State the blood parasite species.
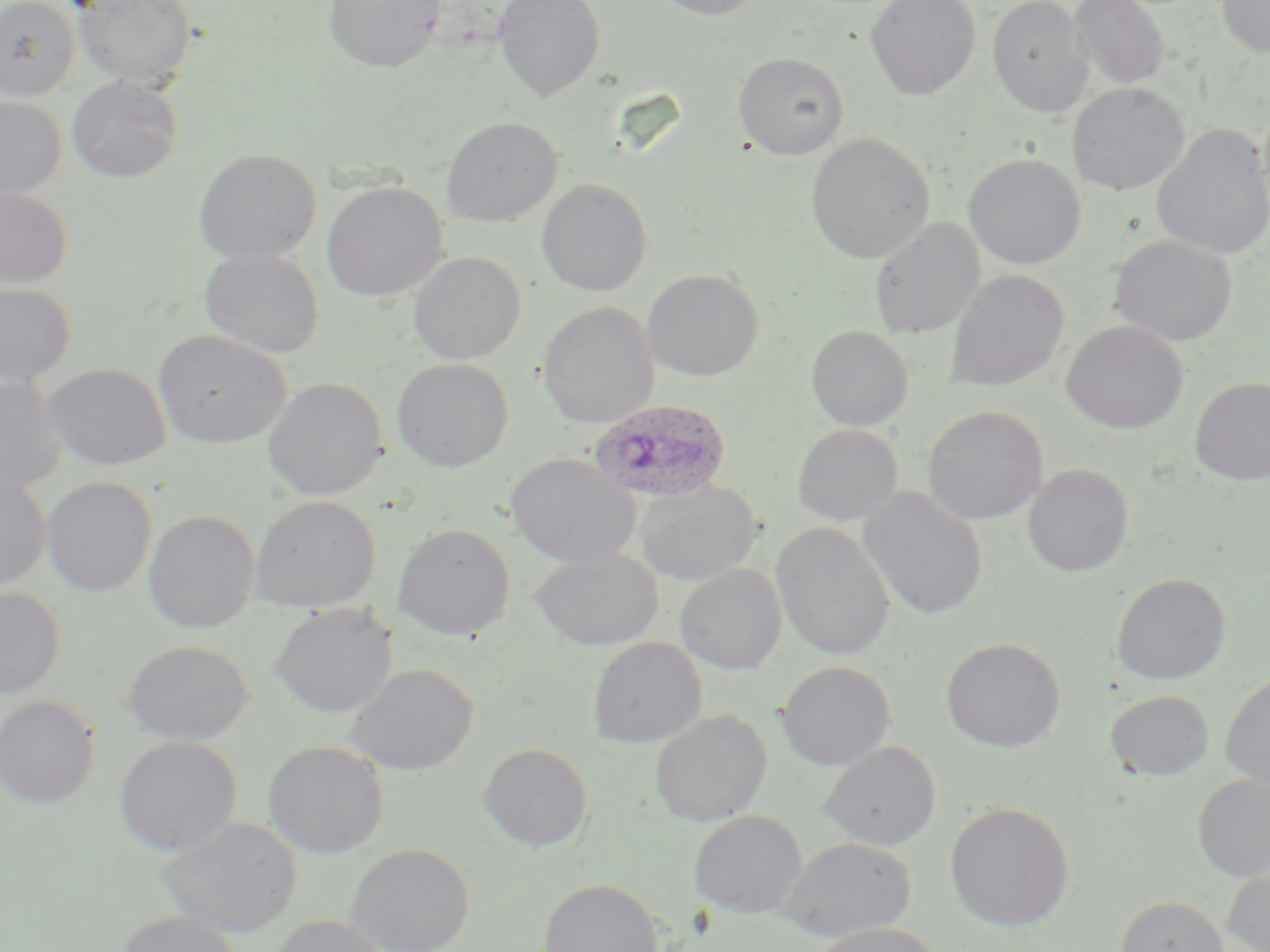

Plasmodium ovale.

Summary:
  - Coordinate format: approximate bounding boxes as (x1, y1, x2, y2) in pixels
  - Uninfected red blood cell locations: (0, 0, 80, 101), (73, 0, 197, 89), (323, 0, 446, 74), (493, 0, 605, 102), (648, 0, 768, 20), (865, 0, 981, 100), (986, 0, 1094, 117), (1068, 0, 1170, 90), (1217, 0, 1270, 58), (733, 51, 849, 159), (66, 76, 185, 184), (1067, 82, 1190, 195), (0, 96, 67, 200), (441, 116, 562, 225), (1151, 123, 1270, 262), (805, 132, 935, 264), (192, 148, 321, 265), (963, 153, 1086, 269), (536, 178, 652, 296), (321, 181, 449, 302), (0, 185, 73, 290), (869, 217, 986, 340), (1109, 233, 1238, 346), (199, 248, 324, 359), (407, 251, 526, 364), (642, 269, 764, 381), (945, 269, 1070, 392), (0, 281, 76, 387), (538, 301, 659, 428), (1061, 320, 1188, 434), (805, 325, 913, 431), (153, 330, 290, 449), (391, 358, 513, 472), (43, 363, 172, 470), (0, 376, 67, 494), (262, 377, 388, 501), (1190, 377, 1270, 485), (923, 405, 1048, 525), (792, 424, 903, 527), (505, 453, 640, 568), (1022, 464, 1134, 577), (0, 471, 51, 593), (42, 476, 157, 597), (635, 481, 761, 585), (857, 486, 988, 620), (248, 495, 381, 613), (143, 510, 260, 634), (770, 522, 895, 661), (392, 523, 516, 640), (531, 547, 663, 651), (675, 564, 786, 674), (1111, 572, 1231, 685), (0, 586, 65, 698), (271, 602, 397, 718), (588, 637, 706, 747), (940, 637, 1066, 752), (123, 640, 252, 745), (777, 660, 896, 770), (346, 664, 478, 774), (1220, 670, 1270, 791), (1104, 690, 1214, 781), (0, 695, 99, 808), (649, 709, 772, 827), (113, 735, 243, 857), (262, 740, 389, 859), (818, 740, 941, 850), (478, 743, 594, 852), (1192, 772, 1270, 882), (945, 801, 1076, 932), (689, 809, 808, 920), (155, 816, 303, 939), (778, 835, 916, 941), (346, 842, 474, 952), (1221, 864, 1270, 952), (539, 878, 662, 952), (1114, 894, 1231, 952), (114, 909, 242, 952), (268, 914, 390, 952), (809, 922, 946, 952)
  - Plasmodium ovale-infected red blood cell locations: (587, 398, 734, 503)
  - Stain: May-Grünwald-Giemsa
  - Preparation: thin blood smear
  - Image size: 1270×952 pixels
  - Field of view: single
  - Magnification: 1000x
  - Modality: light microscopy